Give the position of every Plasmodium falciparum parasite, noting its life-cycle stage.
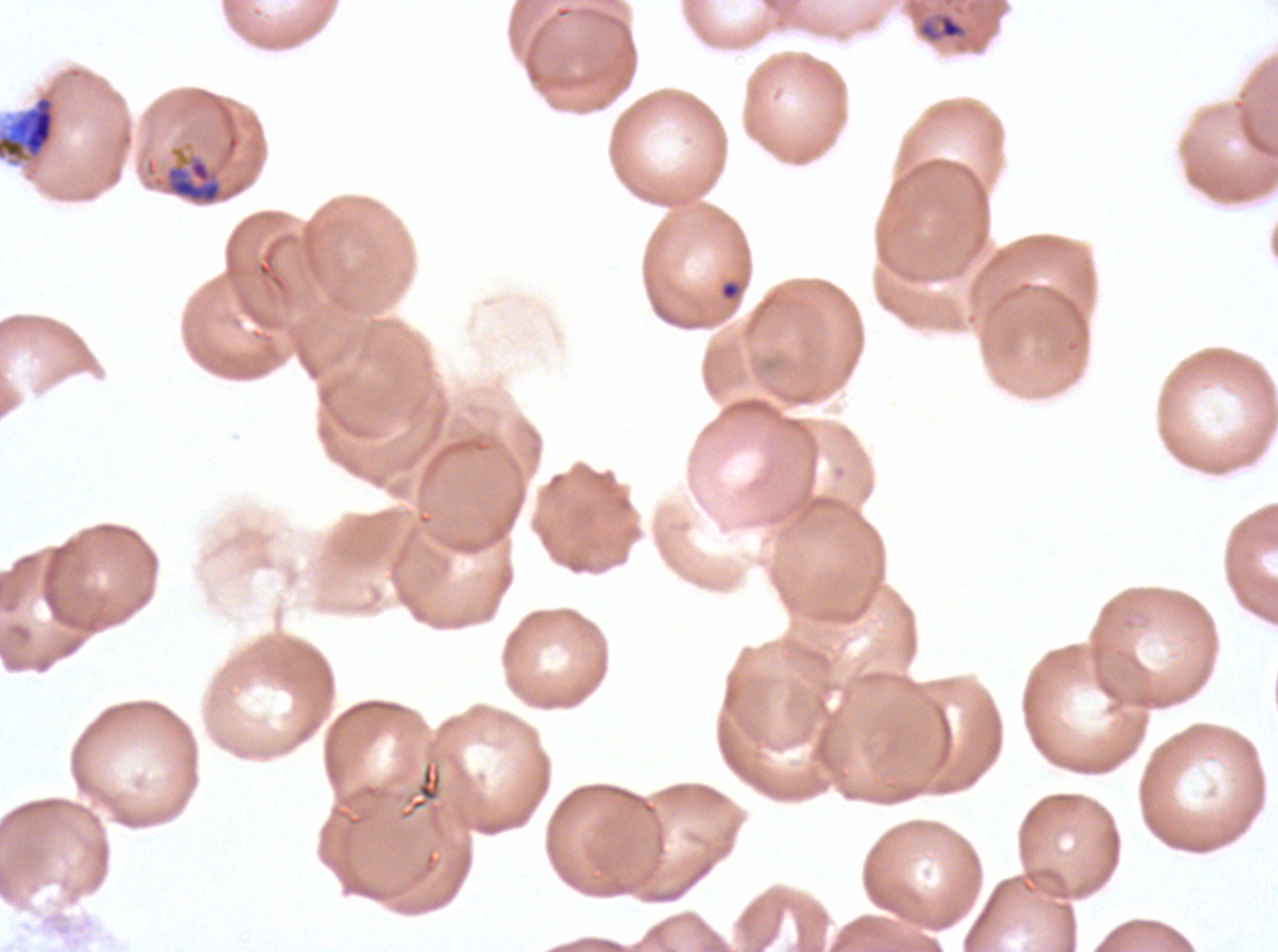
Approximate bounding boxes as (x1, y1, x2, y2) in pixels.
Late-ring/early-trophozoite forms: (916, 12, 967, 43).
Late schizonts: (165, 148, 224, 205).
No rings, mid trophozoites, late trophozoites, early schizonts, segmenters, or gametocytes observed.

field_of_view: one sub-image of a larger composite
image_size: 1278×952 pixels
life_cycle_stages_observed: late-ring/early-trophozoite, late schizont
stain: Giemsa
debris_locations: 'approximate bounding boxes as (x1, y1, x2, y2) in pixels: (0, 93, 58, 164), (719, 280, 741, 301)'
specimen: Plasmodium falciparum from a patient in The Gambia, cultured ex vivo for 24 to 48 hours
preparation: thin blood film